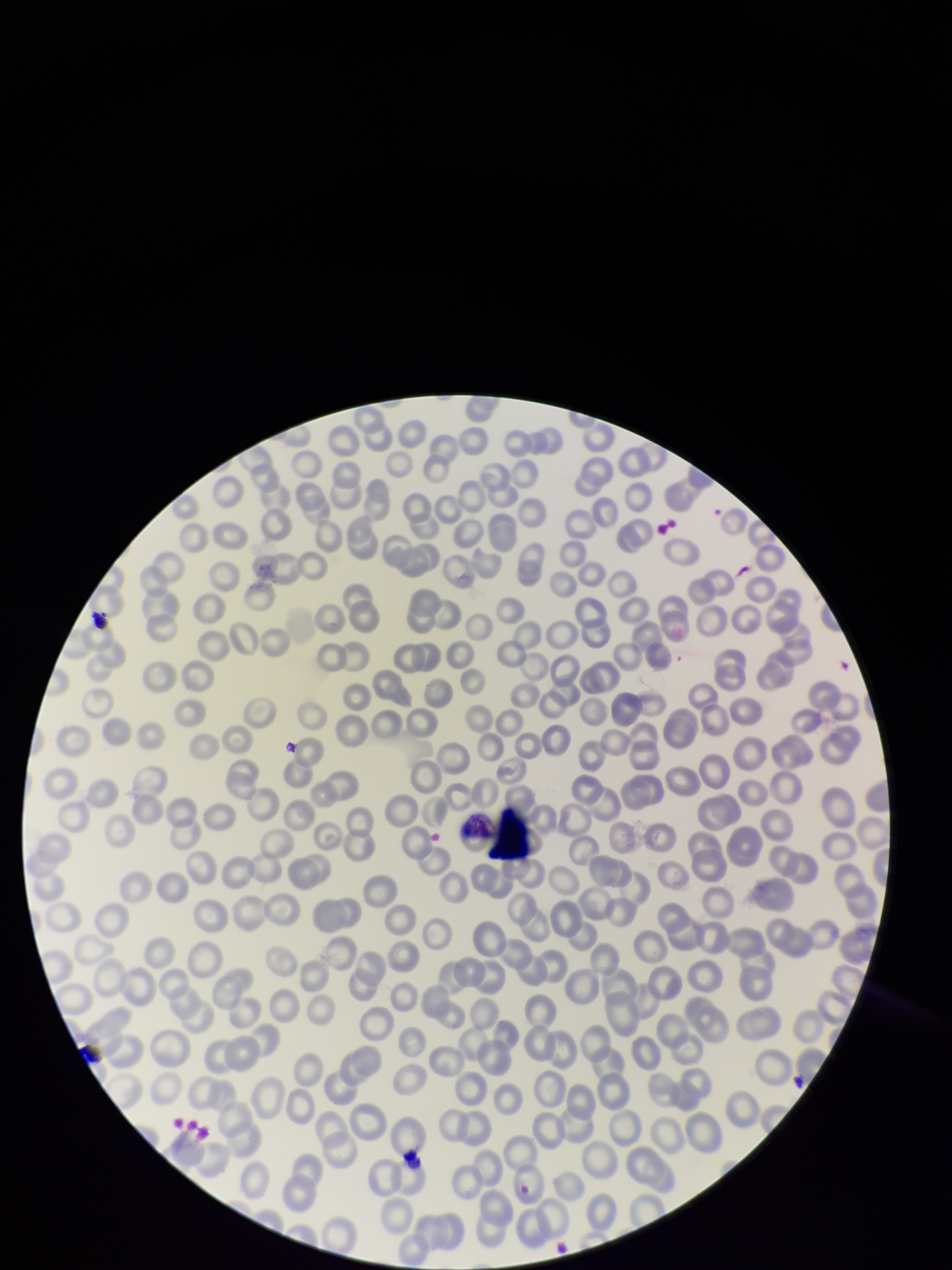

Smartphone photograph taken through the eyepiece of a microscope. Red blood cell count: 231. Preparation: thin blood smear. Patient malaria status: negative. Parasitized red blood cells: none identified. One field from this slide. Stained with Giemsa. Image is 952×1270 pixels. Parasitized red blood cell count: 0.